Give the extent of all uninfected red blood cells.
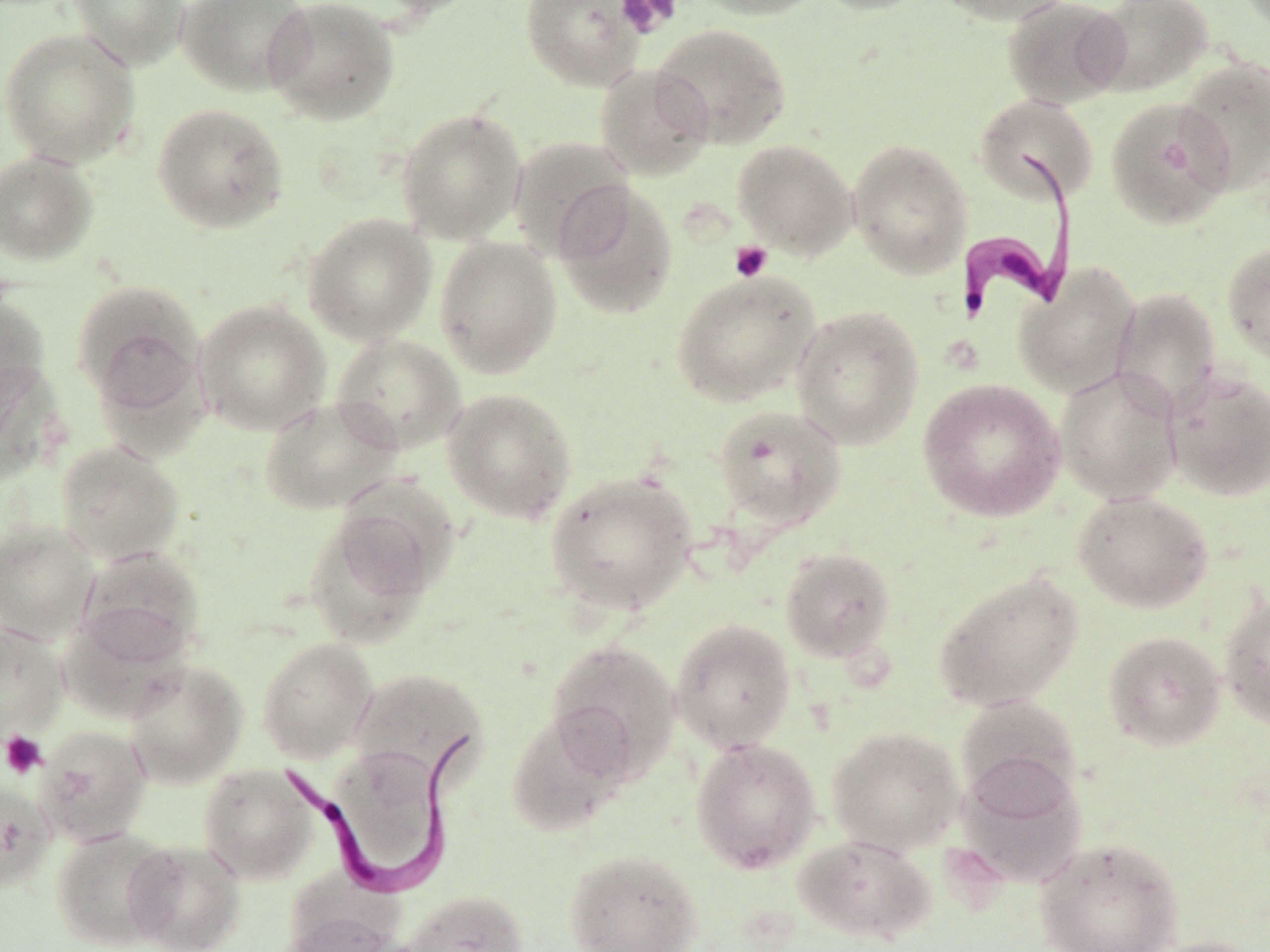

Approximate bounding boxes as [x1, y1, x2, y2] in pixels.
Uninfected red blood cells: [68, 0, 190, 71], [177, 0, 314, 96], [264, 0, 401, 126], [366, 0, 483, 19], [520, 0, 646, 91], [688, 0, 827, 20], [811, 0, 933, 15], [934, 0, 1074, 26], [1002, 0, 1131, 109], [1088, 0, 1215, 96], [651, 22, 792, 149], [0, 28, 140, 166], [1176, 56, 1269, 194], [594, 63, 715, 181], [975, 94, 1099, 206], [1104, 96, 1236, 230], [152, 103, 289, 233], [396, 107, 528, 244], [507, 135, 635, 261], [848, 138, 973, 279], [732, 139, 857, 258], [0, 150, 98, 266], [552, 181, 679, 320], [303, 213, 437, 345], [435, 235, 563, 379], [1222, 240, 1270, 366], [1013, 262, 1141, 398], [670, 268, 821, 407], [73, 279, 205, 417], [1110, 287, 1222, 418], [0, 293, 51, 407], [195, 299, 331, 435], [791, 305, 924, 449], [331, 332, 466, 454], [0, 360, 64, 484], [1055, 366, 1183, 505], [1164, 368, 1270, 502], [917, 377, 1065, 522], [442, 387, 578, 524], [259, 395, 402, 516], [712, 404, 847, 532], [56, 440, 185, 565], [545, 470, 697, 615], [1072, 490, 1214, 613], [302, 508, 439, 650], [0, 519, 99, 644], [778, 546, 896, 664], [75, 547, 205, 668], [933, 571, 1084, 712], [1219, 590, 1270, 731], [670, 618, 797, 753], [0, 623, 69, 742], [1102, 629, 1226, 751], [257, 638, 378, 763], [545, 638, 681, 780], [123, 660, 248, 789], [348, 667, 487, 785], [953, 696, 1083, 807], [506, 709, 630, 838], [35, 724, 153, 847], [827, 726, 965, 854], [690, 737, 821, 874], [955, 754, 1087, 889], [198, 764, 320, 884], [0, 780, 56, 892], [51, 827, 177, 950], [792, 834, 936, 946], [1033, 836, 1184, 952], [123, 839, 247, 952], [564, 848, 703, 952], [402, 889, 527, 952], [279, 894, 403, 952], [1134, 935, 1268, 952].

Summary:
  - Trypanosoma brucei locations: [953, 152, 1081, 325], [283, 733, 474, 896]
  - Platelet locations: [616, 0, 681, 38], [729, 240, 773, 282], [1, 730, 47, 777]
  - Slide-level diagnosis: Trypanosoma brucei
  - Field of view: single
  - Image size: 1270×952 pixels
  - Magnification: 1000x
  - Stain: May-Grünwald-Giemsa
  - Modality: optical microscopy
  - Preparation: thin blood smear